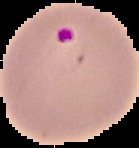

image size = 139×148 pixels
image type = segmented cell region with the area outside set to black
preparation = thin blood film
result = Plasmodium parasites identified